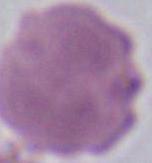 An erythrocyte is seen. Photomicrograph. 1000x magnification.